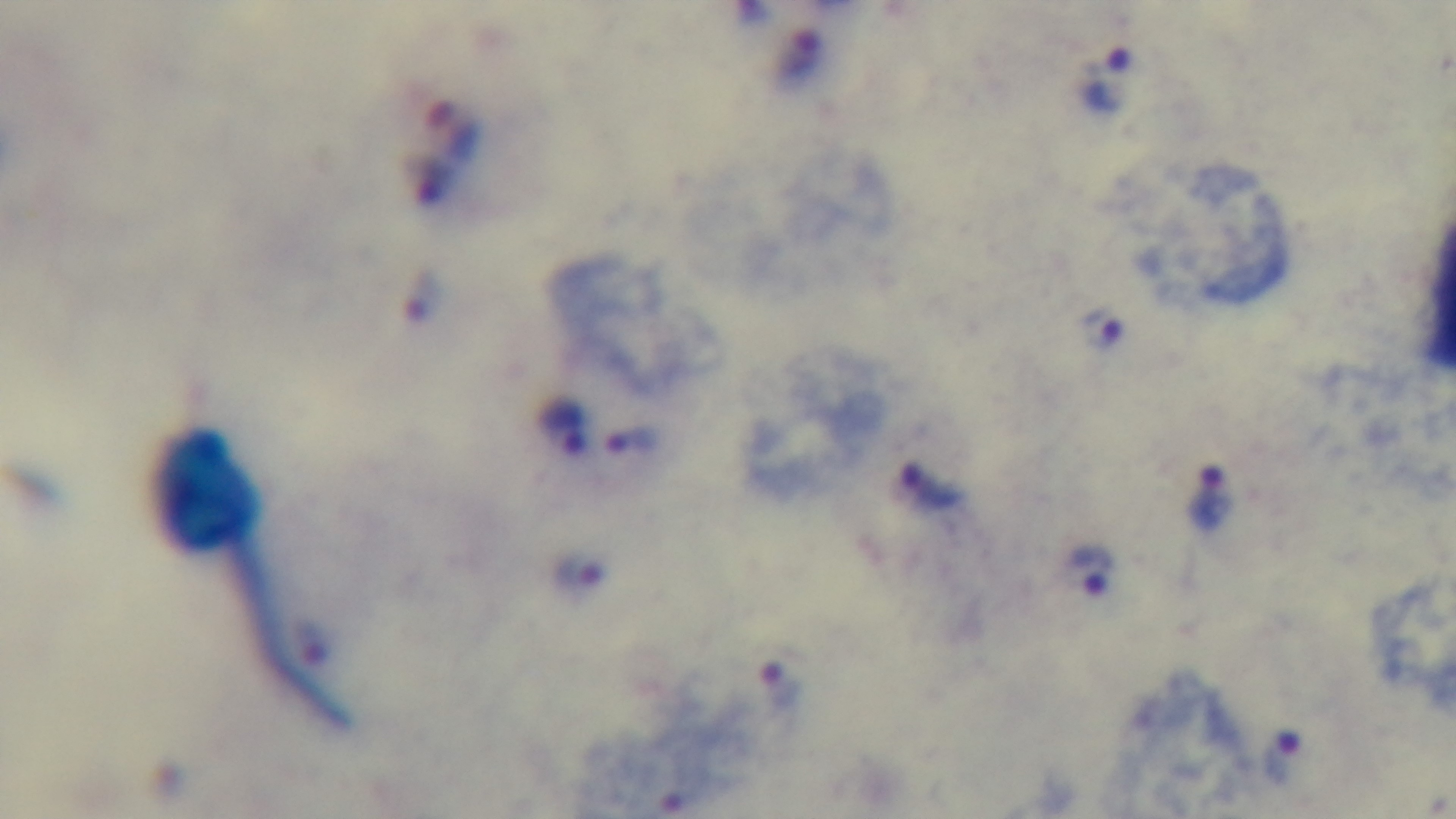

Oil-immersion objective, 100x. Captured with a mounted 4K digital camera. Malaria status: positive. Preparation: thick smear. Giemsa-stained. Photomicrograph. One field from the slide.